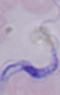
Summary:
  - Identification: trypanosome
  - Magnification: 1000x
  - Modality: micrograph